Classify this cell by malaria status.
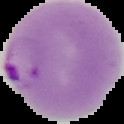
Parasitized.

image type = segmented cell region on a black background
preparation = thin blood film
image size = 124×124 pixels